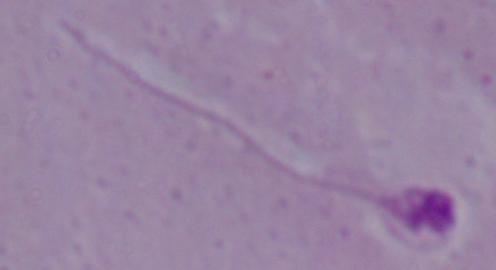
{
  "modality": "micrograph",
  "magnification": "1000x",
  "identification": "Leishmania"
}